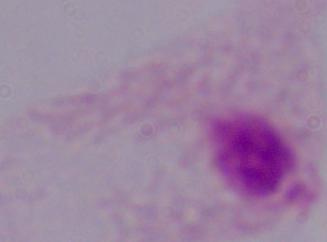

Summary:
  - Magnification: 1000x
  - Identification: trichomonad
  - Modality: micrograph